Assess this cell for malaria.
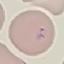
Parasitized.

{
  "capture": "smartphone through the microscope eyepiece",
  "preparation": "thin blood film",
  "stain": "Giemsa",
  "image_type": "cell patch, automatically extracted from a larger field of view and resized to 64 × 64 pixels"
}